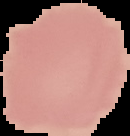

Summary:
  - Image type: cell region segmented out of the field of view; surrounding area masked to black
  - Image size: 130×136 pixels
  - Malaria status: uninfected
  - Preparation: thin blood smear